Classify this cell by malaria status.
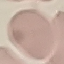

It is uninfected.

Automatically extracted cell patch, resized to 64 × 64 pixels. Photographed with a smartphone camera at the microscope eyepiece. Thin blood film. Giemsa-stained preparation.